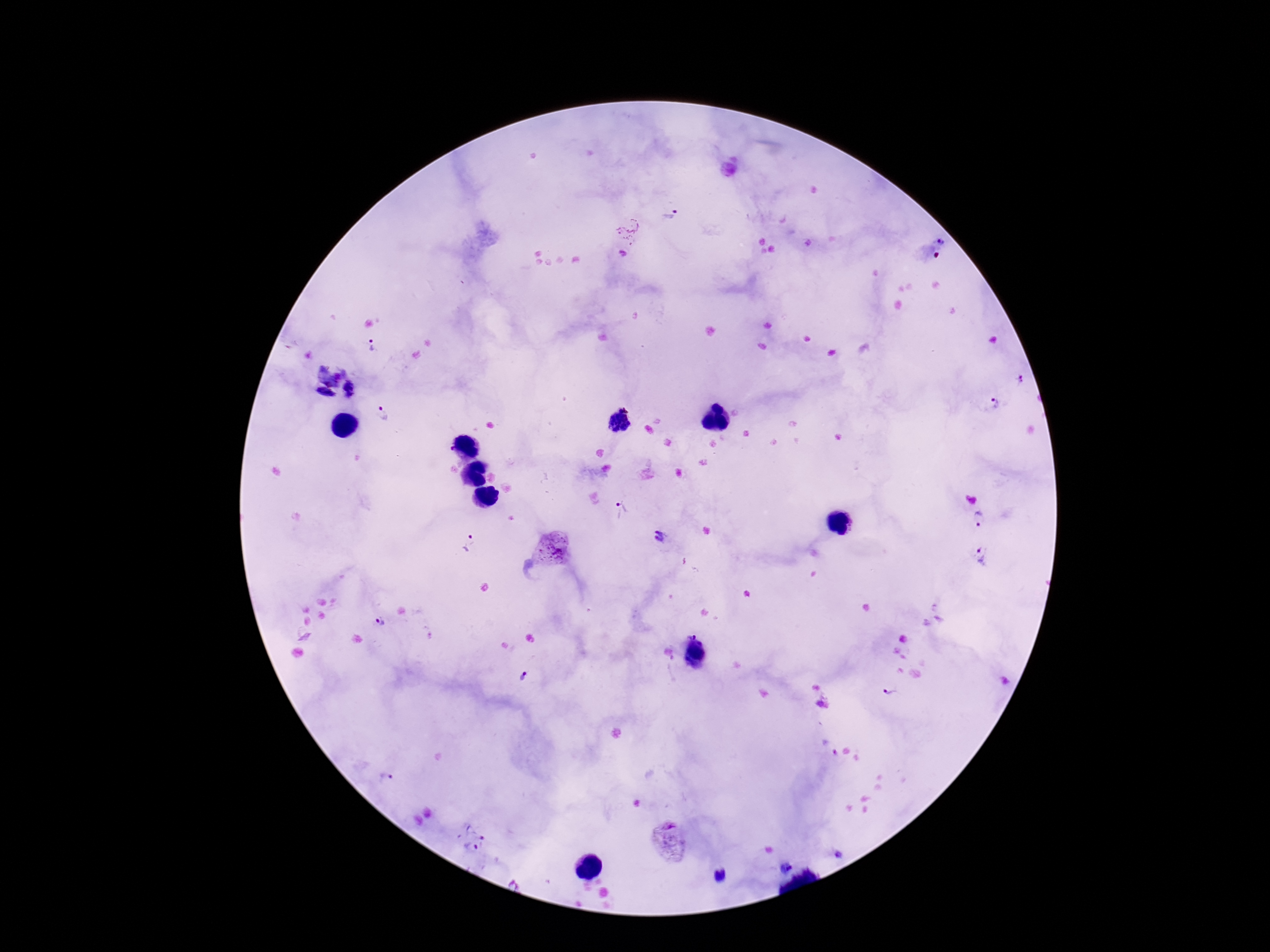

Approximate centers as (x, y) in pixels. Plasmodium parasite locations: (672, 215), (628, 229), (941, 242), (623, 254), (372, 344), (329, 372), (1021, 378), (352, 390), (323, 401), (996, 403), (383, 414), (621, 509), (980, 518), (658, 535), (471, 543), (553, 549), (984, 555), (377, 619), (692, 633), (698, 655), (525, 677), (890, 691), (386, 780), (481, 837), (667, 841), (471, 847), (842, 853), (784, 866), (721, 876). Image is 1270×952 pixels. Thick blood film. Smartphone photograph taken through the microscope eyepiece. 100x magnification. Giemsa stain. Patient malaria status: positive. Single field of view.